Draw a bounding box around every leukocyte (white blood cell).
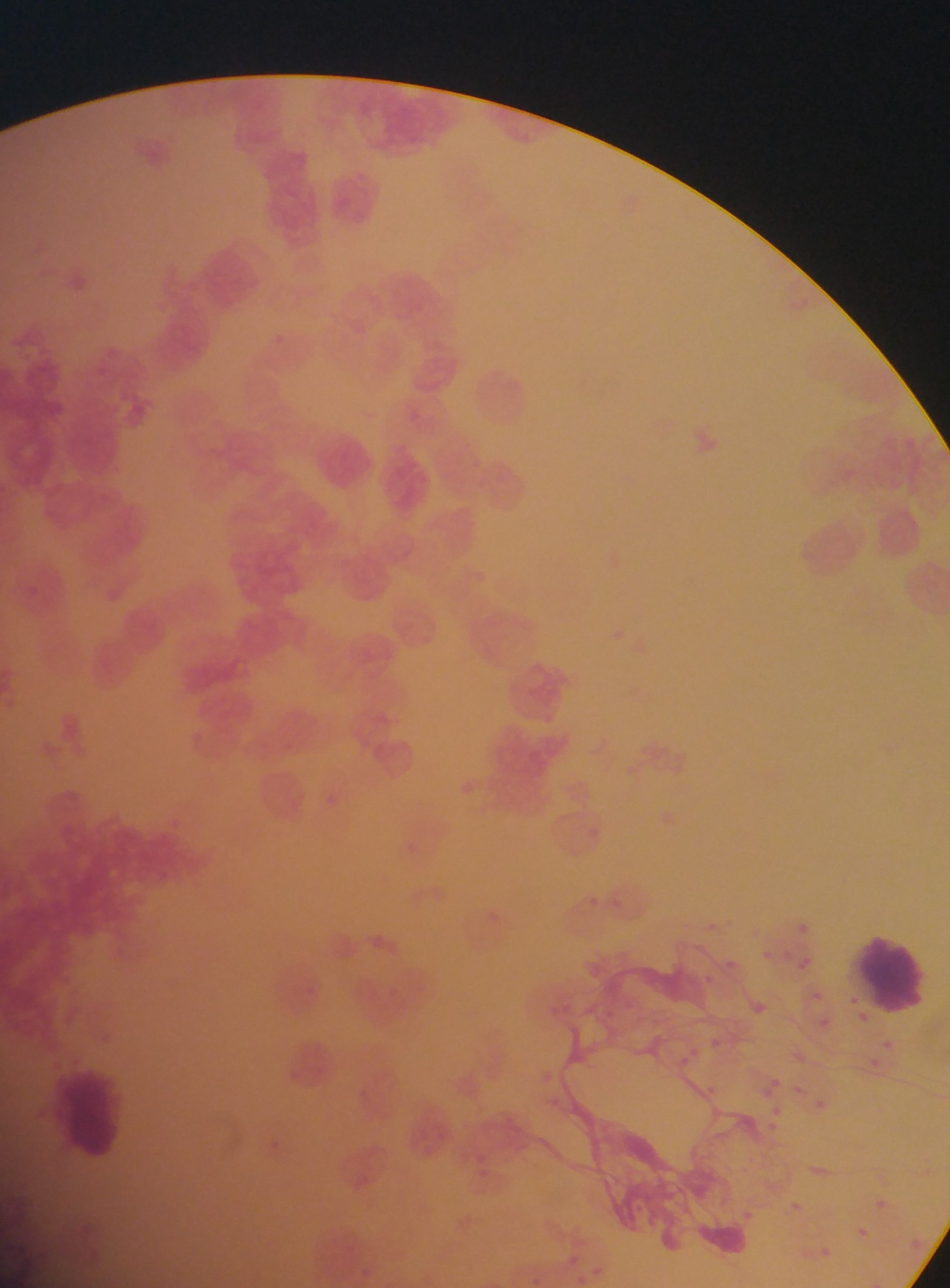

Approximate bounding boxes as {left, top, right, bottom} in pixels.
Leukocytes: {855, 927, 932, 1014}, {53, 1060, 126, 1155}.

Summary:
  - Capture: mobile-phone photograph through a microscope
  - Image size: 950×1288 pixels
  - Field of view: single
  - Preparation: thin blood film
  - Country: Ghana